Describe the morphology of the erythrocytes.
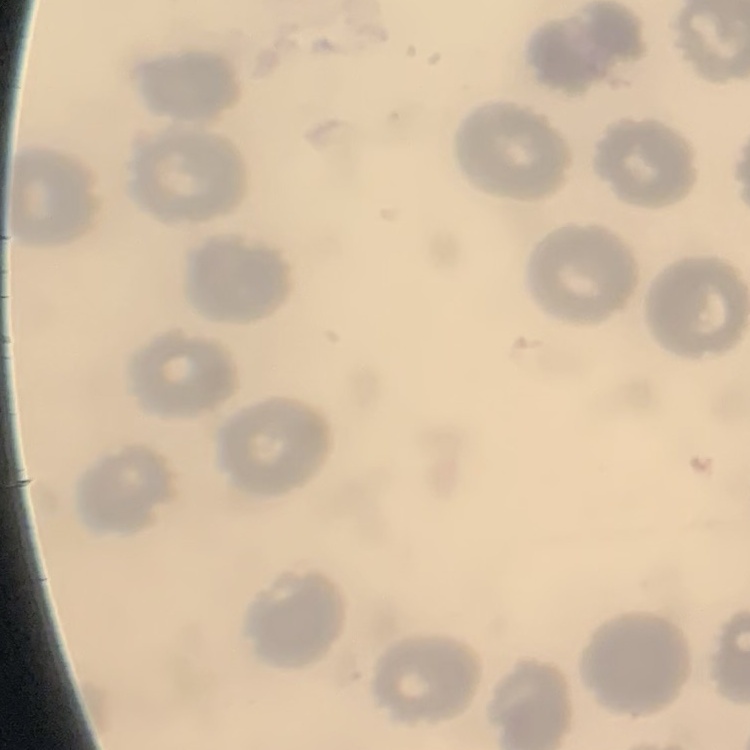

They show no rouleaux formation.

One tile cut from a larger photomicrograph. Field's or Giemsa stain. Thin peripheral smear.